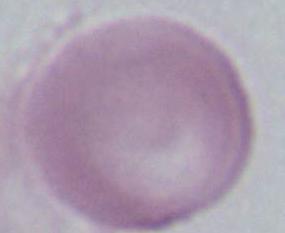
Summary:
  - Identification: erythrocyte
  - Modality: photomicrograph
  - Magnification: 1000x